Assess this cell for malaria.
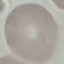

Uninfected.

Acquired by smartphone through the microscope eyepiece. Thin blood smear. Automatically extracted cell patch, resized to 64 × 64 pixels. Giemsa stain.